Assess the morphology of the erythrocytes.
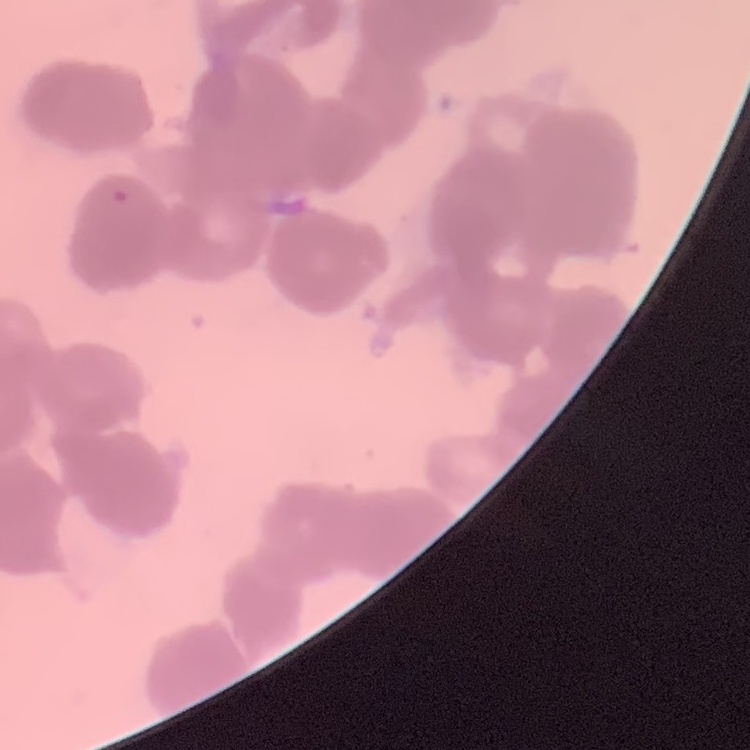
Rouleaux formation.

{
  "stain": "Field's or Giemsa",
  "preparation": "thin peripheral smear",
  "image_type": "one tile cut from a larger photomicrograph"
}